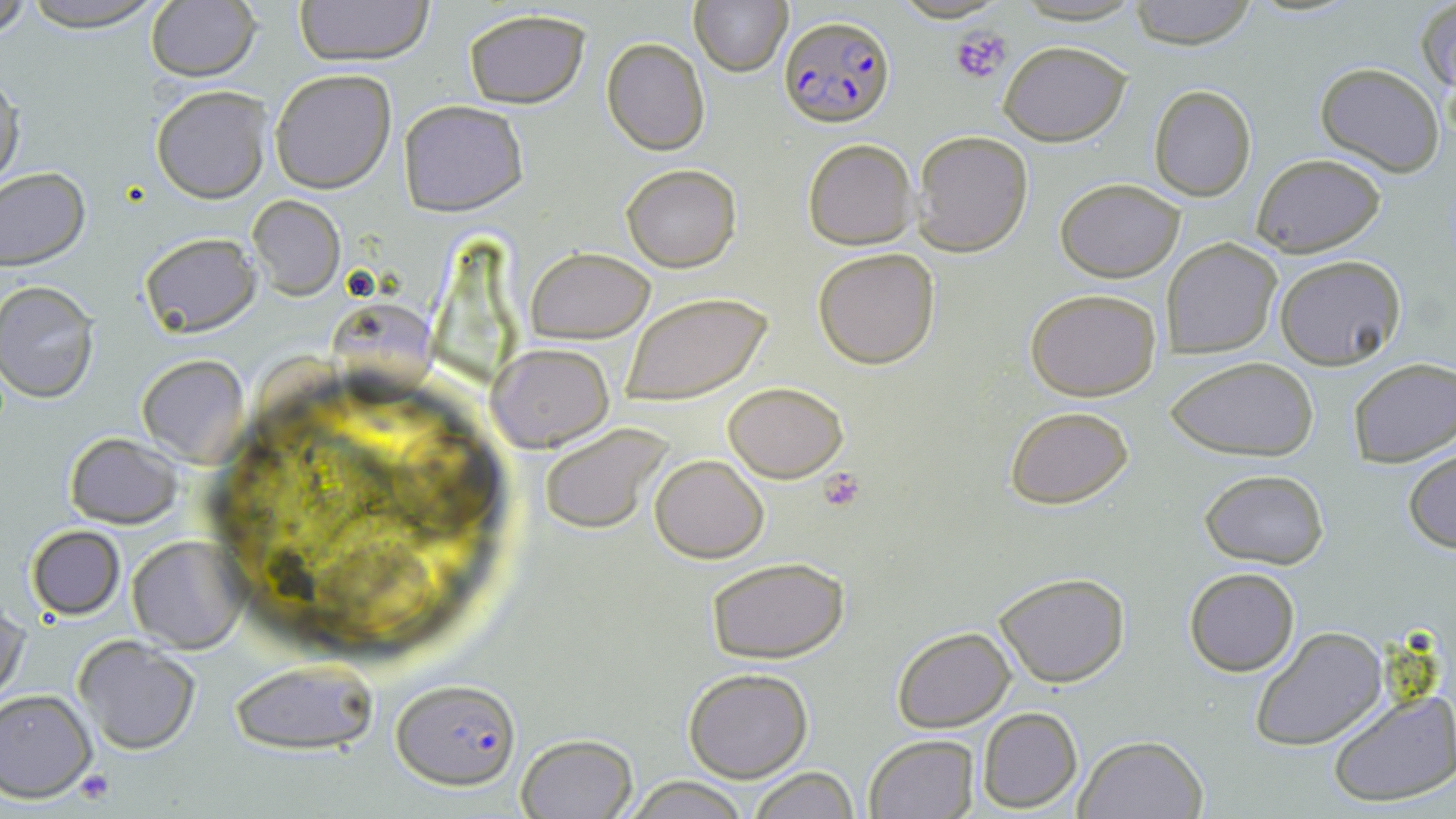
Summary:
  - Coordinate format: approximate bounding boxes as [x1, y1, x2, y2] in pixels
  - Uninfected red blood cell locations: [0, 0, 34, 41], [20, 0, 168, 30], [293, 0, 434, 65], [1128, 0, 1257, 48], [691, 1, 790, 76], [1416, 2, 1455, 94], [145, 3, 259, 81], [462, 9, 592, 108], [600, 37, 711, 156], [999, 40, 1131, 146], [1315, 61, 1445, 175], [270, 68, 396, 193], [0, 71, 24, 195], [151, 85, 268, 203], [1150, 85, 1258, 201], [399, 100, 528, 216], [915, 130, 1034, 257], [802, 138, 917, 248], [1250, 152, 1388, 256], [621, 164, 741, 273], [0, 167, 90, 270], [1056, 179, 1185, 281], [248, 195, 345, 300], [141, 232, 260, 337], [1164, 239, 1282, 357], [813, 247, 942, 369], [526, 248, 654, 343], [1274, 254, 1406, 369], [0, 281, 100, 402], [1025, 287, 1163, 402], [620, 290, 773, 407], [324, 301, 444, 416], [489, 342, 613, 451], [137, 354, 249, 464], [1167, 356, 1319, 460], [1348, 357, 1456, 466], [724, 382, 849, 482], [1005, 405, 1133, 510], [539, 423, 675, 536], [63, 433, 182, 528], [1404, 449, 1456, 553], [651, 455, 768, 562], [1199, 469, 1331, 568], [26, 525, 125, 620], [127, 535, 246, 654], [706, 556, 849, 664], [1184, 567, 1298, 676], [990, 572, 1133, 688], [1, 603, 28, 705], [892, 626, 1016, 731], [1249, 627, 1389, 752], [74, 635, 201, 755], [230, 659, 378, 756], [683, 668, 811, 782], [0, 689, 97, 800], [1326, 690, 1456, 810], [976, 708, 1082, 812], [515, 733, 638, 818], [863, 734, 979, 819], [1073, 734, 1208, 818], [749, 767, 859, 819], [624, 774, 749, 818]
  - Platelet locations: [950, 25, 1014, 87], [817, 466, 868, 511], [73, 769, 113, 806]
  - Plasmodium falciparum-infected red blood cell locations: [778, 15, 896, 129], [391, 678, 520, 789]
  - Slide-level diagnosis: Plasmodium falciparum
  - Magnification: 1000x
  - Stain: May-Grünwald-Giemsa
  - Preparation: thin blood smear
  - Modality: light microscopy
  - Image size: 1456×819 pixels
  - Field of view: single